State which cell type is depicted.
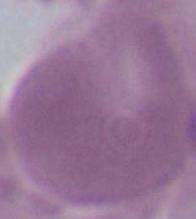

An erythrocyte.

Summary:
  - Modality: photomicrograph
  - Magnification: 1000x